Assess this cell for malaria.
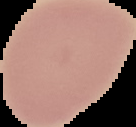

It is uninfected.

Summary:
  - Image type: cell region segmented out of the field of view; surrounding area masked to black
  - Preparation: thin blood film
  - Image size: 136×127 pixels